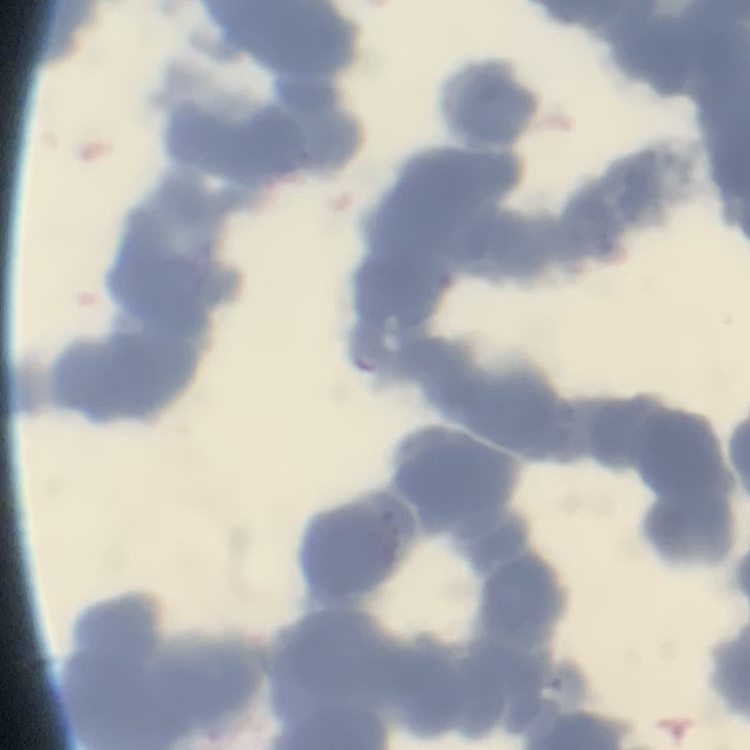

The red blood cells show rouleaux formation. One tile cut from a larger photomicrograph. Thin peripheral smear. Field's or Giemsa stain.